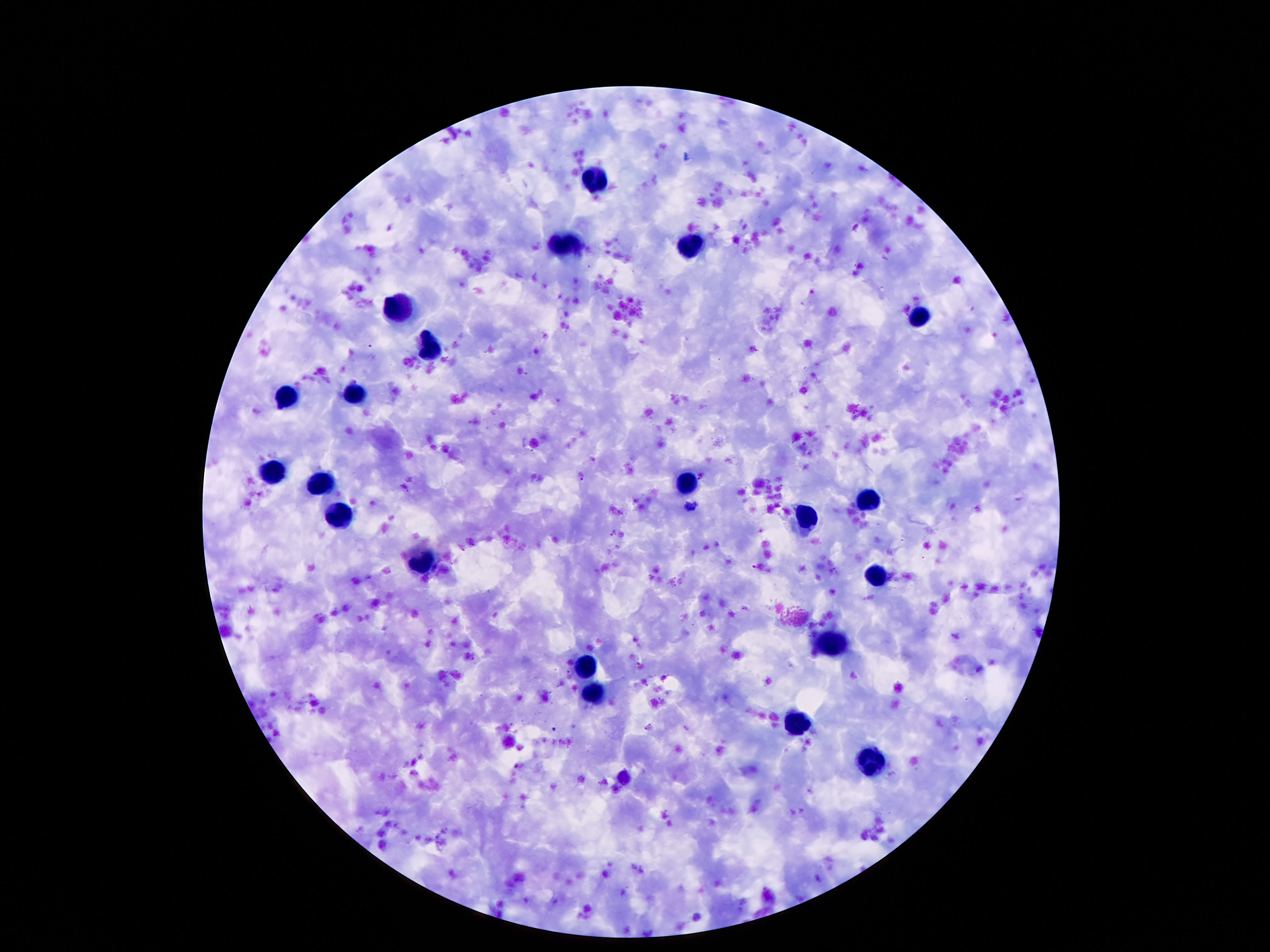
Approximate centers as (x, y) in pixels. Leukocyte locations: (597, 180), (690, 245), (567, 246), (401, 310), (922, 319), (429, 347), (352, 394), (289, 396), (274, 472), (687, 480), (321, 485), (868, 500), (341, 515), (804, 519), (425, 563), (879, 573), (831, 644), (586, 666), (595, 694), (795, 721), (870, 762). Giemsa stain. Thick blood smear. One field from this slide. Smartphone photograph taken through the microscope eyepiece. Image is 1270×952 pixels. 100x magnification. Patient malaria status: negative.